Mark where leukocytes are.
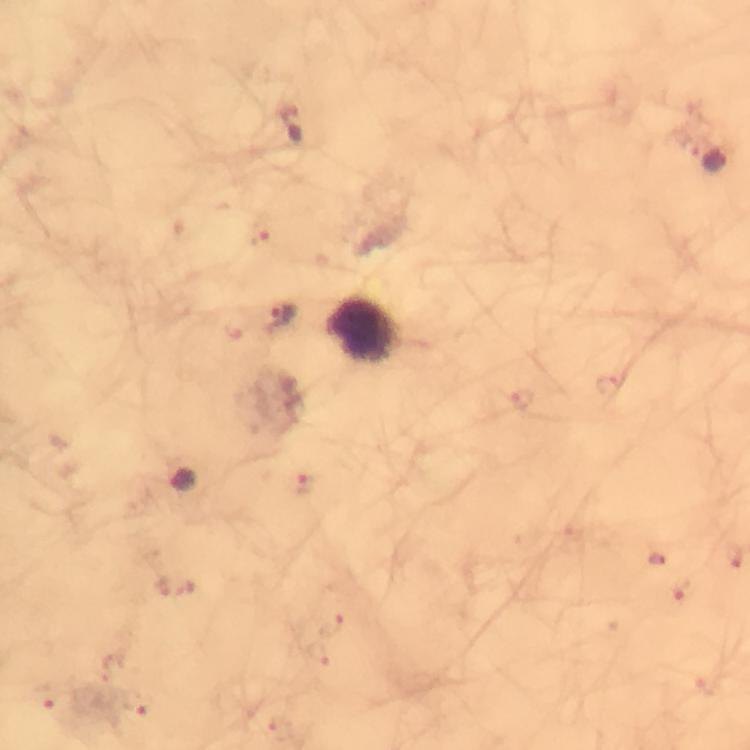
Approximate centers as [x, y] in pixels.
Leukocytes: [370, 333].

Plasmodium parasite locations: [292, 123], [714, 160], [282, 319], [184, 480]. From a diagnostic examination for malaria. Immersion oil applied. Giemsa-stained preparation. Photographed through the microscope with a smartphone camera. 100x magnification. Thick smear. Image is 750×750 pixels. A crop from one field of view.